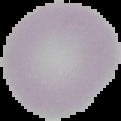
Malaria status: uninfected. Segmented cell region on a black background. Image is 121×121 pixels. From a thin blood film.